Comment on the morphology of the erythrocytes.
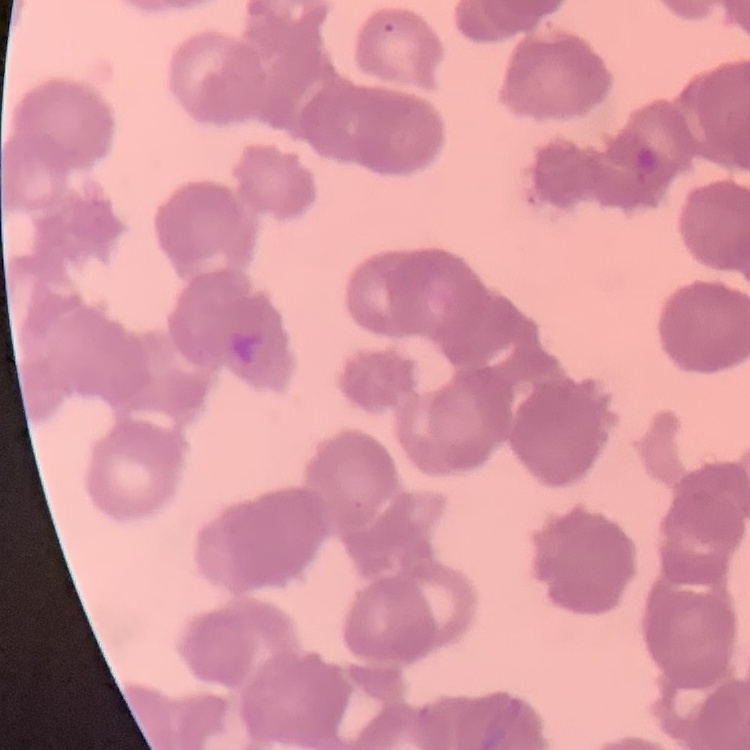
Rouleaux formation.

One tile cut from a larger photomicrograph. Stained with either Field's or Giemsa. Thin blood smear.